Assess this cell for malaria.
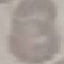

It is uninfected.

preparation: thin blood film
image_type: cell patch, automatically extracted from a larger field of view and resized to 64 × 64 pixels
capture: smartphone camera at the microscope eyepiece
stain: Giemsa